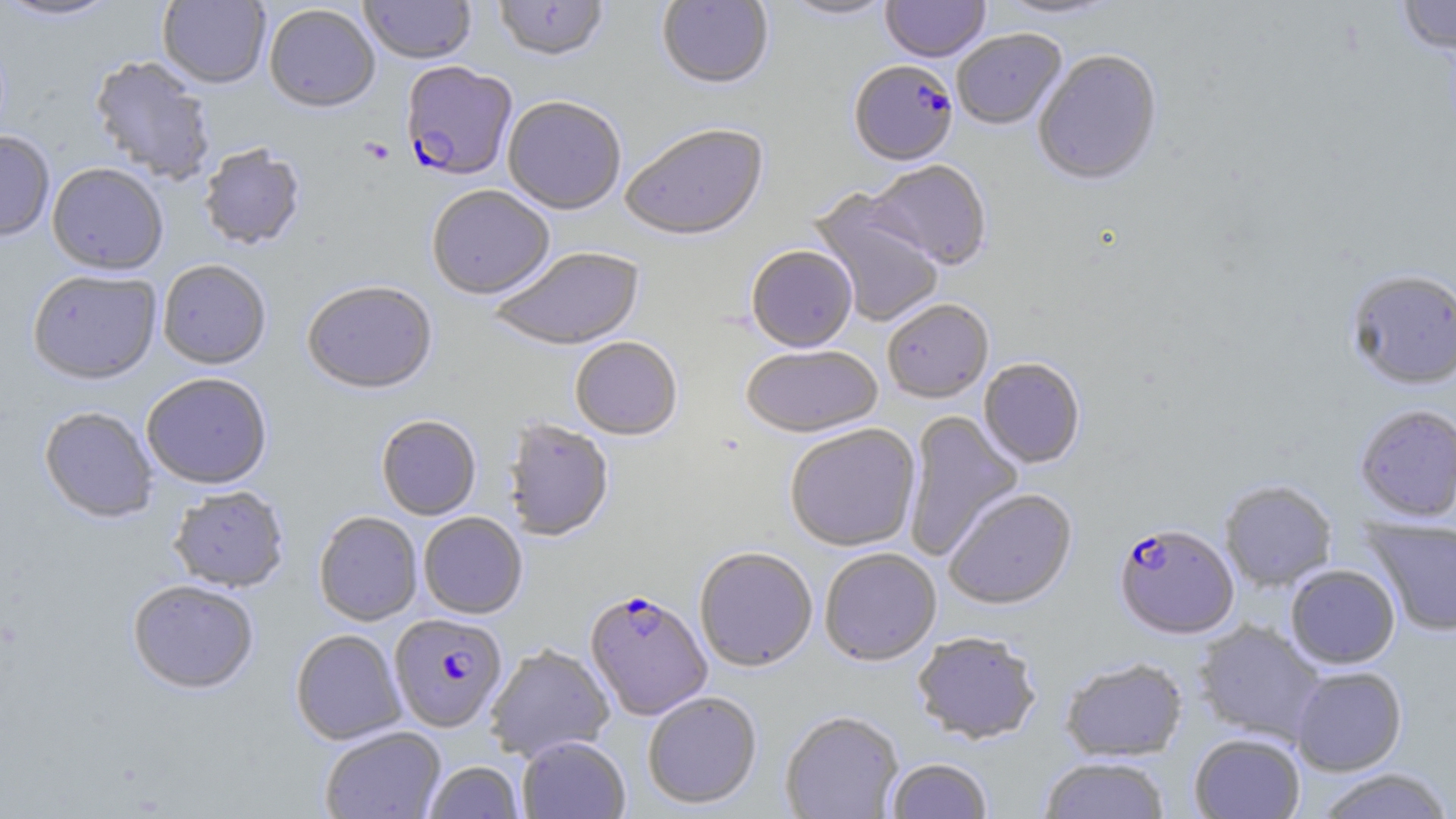

Plasmodium falciparum-infected red blood cell locations = approximate bounding boxes as (x1,y1)-(x2,y2) corner pairs in pixels: (848,62)-(958,168), (401,63)-(518,184), (1114,523)-(1239,639), (584,590)-(713,720), (389,614)-(507,733)
slide-level diagnosis = Plasmodium falciparum
preparation = thin blood smear
modality = optical microscopy
image size = 1456×819 pixels
field of view = one of a larger specimen
stain = May-Grünwald-Giemsa
platelet locations = approximate bounding boxes as (x1,y1)-(x2,y2) corner pairs in pixels: (359,137)-(395,166)
magnification = 1000x
uninfected red blood cell locations = approximate bounding boxes as (x1,y1)-(x2,y2) corner pairs in pixels: (0,0)-(121,23), (157,0)-(270,89), (359,0)-(476,65), (493,0)-(608,64), (657,0)-(774,92), (781,0)-(896,22), (881,0)-(989,64), (993,0)-(1125,22), (1397,0)-(1456,56), (264,5)-(380,115), (952,31)-(1067,132), (1033,51)-(1163,189), (88,56)-(216,185), (503,98)-(625,216), (621,126)-(770,243), (0,131)-(54,242), (198,145)-(306,252), (864,162)-(993,271), (47,164)-(168,276), (427,187)-(555,302), (807,189)-(945,327), (746,247)-(857,353), (490,248)-(646,352), (157,260)-(271,371), (1345,270)-(1456,390), (28,272)-(161,386), (302,282)-(437,396), (882,301)-(994,404), (570,338)-(683,442), (741,346)-(884,439), (979,359)-(1085,469), (141,374)-(273,490), (1354,405)-(1456,523), (39,407)-(158,524), (903,411)-(1023,561), (376,415)-(482,520), (503,420)-(614,542), (784,424)-(921,553), (1219,480)-(1337,592), (168,487)-(290,593), (943,489)-(1078,611), (313,511)-(423,626), (418,513)-(527,619), (1363,517)-(1456,636), (694,548)-(817,672), (820,549)-(941,667), (1286,565)-(1400,669), (127,579)-(259,695), (1194,621)-(1325,743), (290,629)-(406,745), (912,632)-(1042,745), (485,644)-(615,762), (1060,658)-(1188,761), (1290,666)-(1407,776), (643,691)-(762,810), (780,711)-(904,819), (319,726)-(446,818), (1189,733)-(1305,819), (517,736)-(631,819), (1040,756)-(1171,819), (887,758)-(992,818), (423,761)-(525,819), (1312,769)-(1454,819)